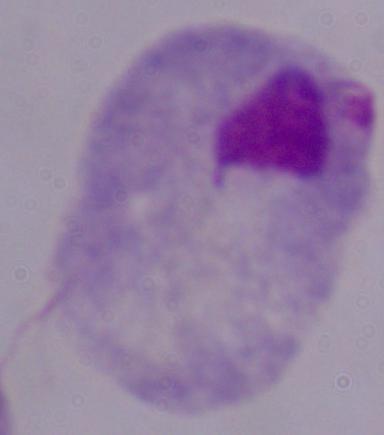

Captured at 1000x magnification. Micrograph. A trichomonad is seen.